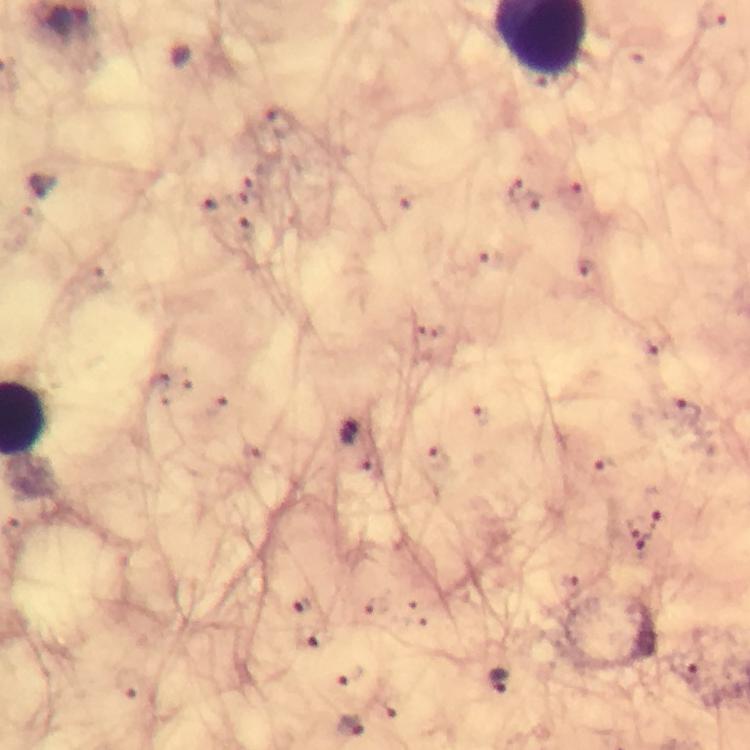
stain: Giemsa
preparation: thick blood film
capture: smartphone camera through the microscope
magnification: 100x
image_size: 750×750 pixels
cropped_from: a single field of view
immersion_oil: used
context: from a diagnostic examination for malaria
plasmodium_parasite_locations: 'approximate centers as {x, y} in pixels: {520, 192}, {688, 415}, {348, 433}, {634, 525}, {304, 603}, {319, 637}, {687, 672}, {498, 680}, {351, 725}'